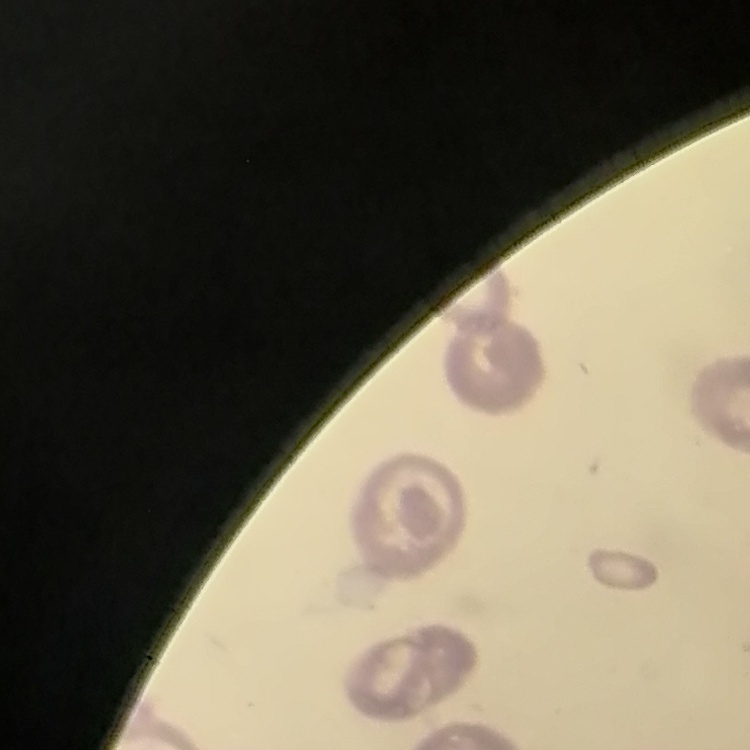

Summary:
  - Red blood cell morphology: no rouleaux formation
  - Preparation: thin blood film
  - Stain: Field's or Giemsa
  - Image type: square crop of a larger photomicrograph